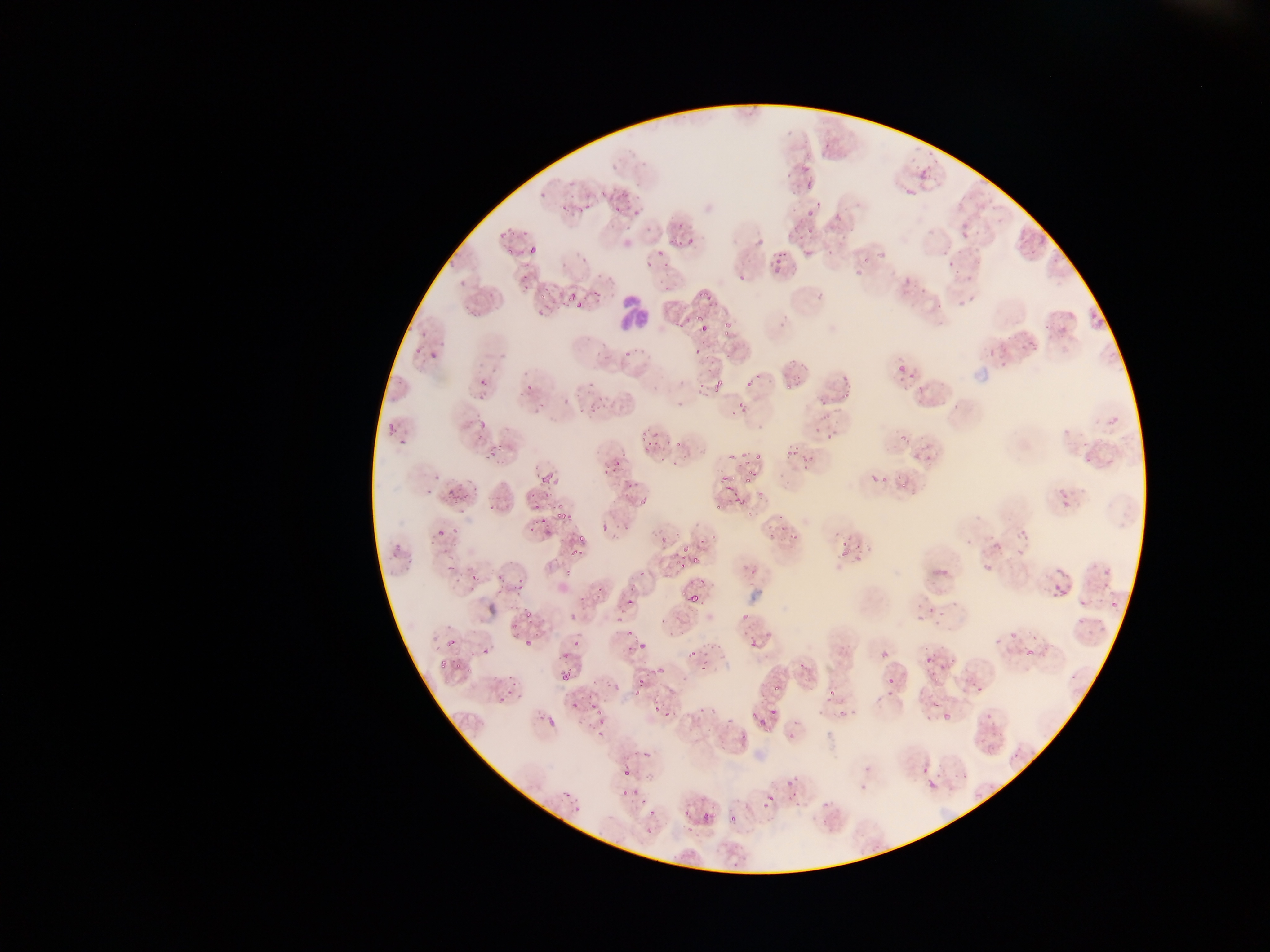

Approximate bounding boxes as left top right bottom in pixels. Malaria parasite locations: 800 154 826 206; 913 160 932 184; 899 186 916 201; 607 190 637 228; 790 202 814 230; 958 222 983 256; 525 230 545 254; 766 250 788 277; 946 250 967 269; 845 255 872 279; 511 268 537 291; 900 273 915 295; 696 281 717 325; 952 285 983 310; 539 293 577 312; 724 314 745 340; 1043 316 1075 338; 699 325 708 334; 1016 332 1040 364; 989 344 1010 370; 891 358 917 388; 780 364 812 388; 841 373 862 395; 476 379 491 398; 707 383 728 403; 584 398 607 418; 738 400 748 411; 474 415 490 433; 1101 417 1125 430; 644 432 665 455; 896 433 911 446; 484 440 510 470; 913 440 933 464; 1081 445 1100 465; 786 448 796 458; 601 455 623 474; 863 461 889 489; 535 464 559 482; 895 466 914 488; 715 469 743 497; 744 470 760 490; 444 485 474 503; 731 488 752 511; 1056 492 1079 511; 524 493 540 509; 551 503 571 520; 537 515 544 530; 1011 521 1038 558; 779 523 798 544; 432 524 443 537; 566 531 592 557; 841 533 854 554; 666 545 686 563; 980 549 997 578; 692 556 699 565; 1093 562 1117 598; 458 564 484 590; 1051 565 1077 591; 494 572 518 592; 1050 585 1067 602; 621 590 645 612; 1071 592 1097 634; 690 593 698 602; 1104 593 1125 617; 520 601 535 621; 913 601 935 627; 558 604 584 623; 509 613 518 632; 990 622 1019 643; 742 623 769 659; 517 626 538 654; 441 632 461 663; 637 633 650 653; 1024 637 1040 656; 922 638 939 680; 689 642 723 674; 478 645 494 656; 558 646 575 661; 881 651 889 658; 935 660 957 676; 561 672 570 680; 635 674 654 696; 968 676 985 696; 887 677 895 687; 494 679 518 707; 817 688 849 715; 563 696 580 711; 580 699 604 718; 647 700 675 722; 753 700 783 732; 698 703 715 727; 728 704 741 723; 939 706 962 727; 547 716 556 728; 592 719 610 747; 912 753 934 777; 615 764 637 785; 923 766 945 798; 779 778 804 798; 617 784 634 799; 757 788 778 808; 818 799 844 823; 631 808 657 838; 683 809 693 819; 729 815 738 823. Leukocyte locations: 600 295 646 345. One field of view. Sample from Ghana. Thin blood film. Image is 1270×952 pixels. Mobile-phone photograph taken through the microscope.